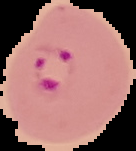

Summary:
  - Image type: cell region segmented out of the field of view; surrounding area masked to black
  - Result: Plasmodium parasites identified
  - Image size: 136×151 pixels
  - Preparation: thin blood smear